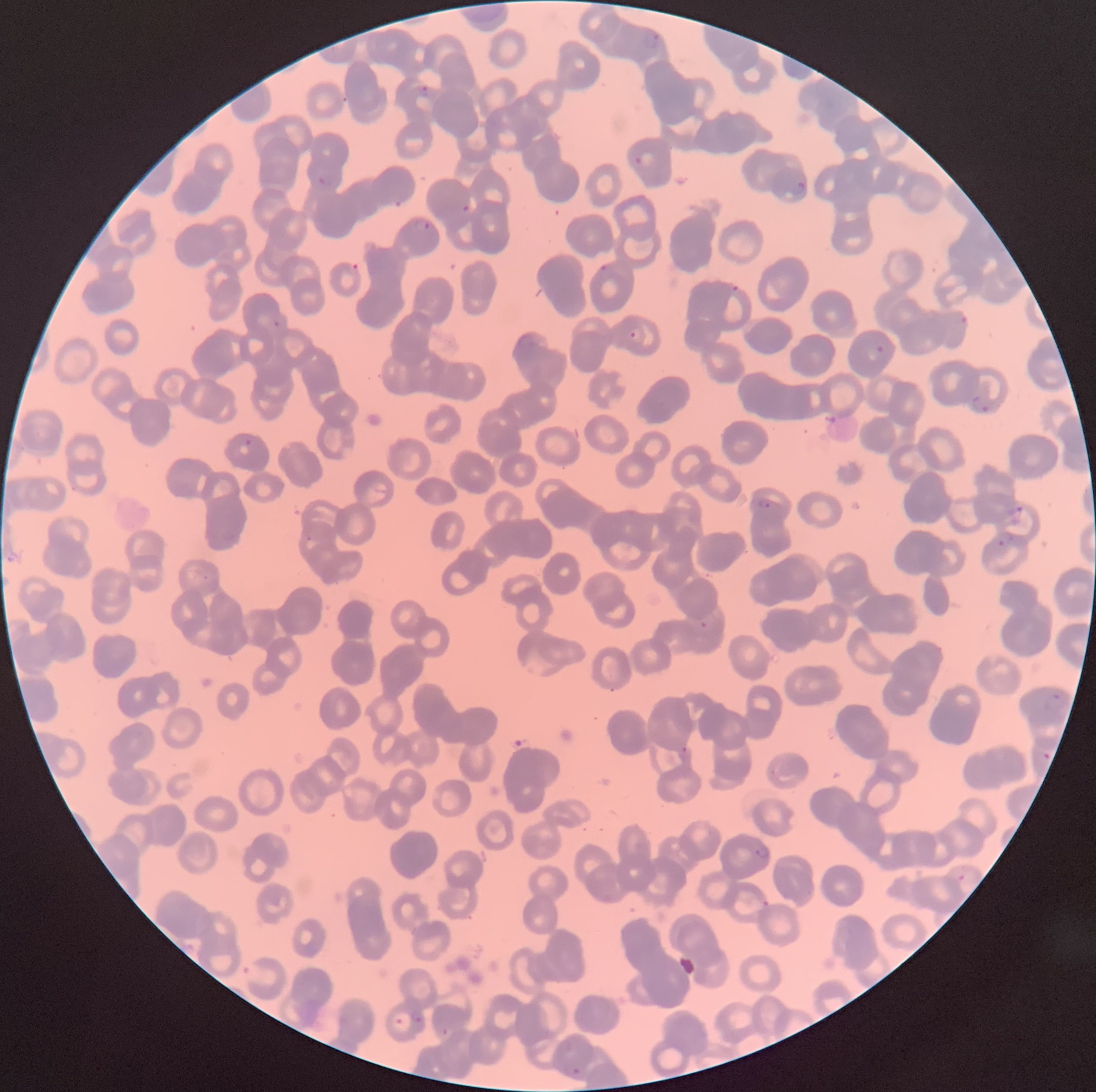
Approximate bounding boxes as [x1, y1, x2, y2] in pixels. Plasmodium parasite locations: [642, 30, 662, 50], [412, 85, 428, 99], [633, 150, 654, 168], [316, 174, 334, 191], [793, 181, 807, 196], [460, 204, 470, 213], [414, 219, 432, 232], [596, 261, 614, 278], [348, 263, 364, 274], [730, 283, 740, 294], [957, 314, 970, 328], [270, 319, 281, 329], [628, 328, 641, 343], [874, 344, 887, 355], [969, 396, 993, 414], [244, 438, 253, 447], [757, 498, 773, 510], [1006, 504, 1023, 526], [997, 532, 1016, 548], [305, 535, 313, 543], [699, 620, 710, 629], [1044, 689, 1067, 710], [679, 745, 690, 755], [1040, 750, 1053, 762], [754, 845, 772, 861], [957, 873, 967, 882], [761, 899, 770, 908], [241, 961, 261, 984], [408, 1011, 423, 1023], [395, 1017, 404, 1026], [440, 1026, 449, 1035], [562, 1062, 582, 1080]. The red blood cells show rouleaux formation. Thin blood smear. Optical microscopy. Image is 1096×1092 pixels.